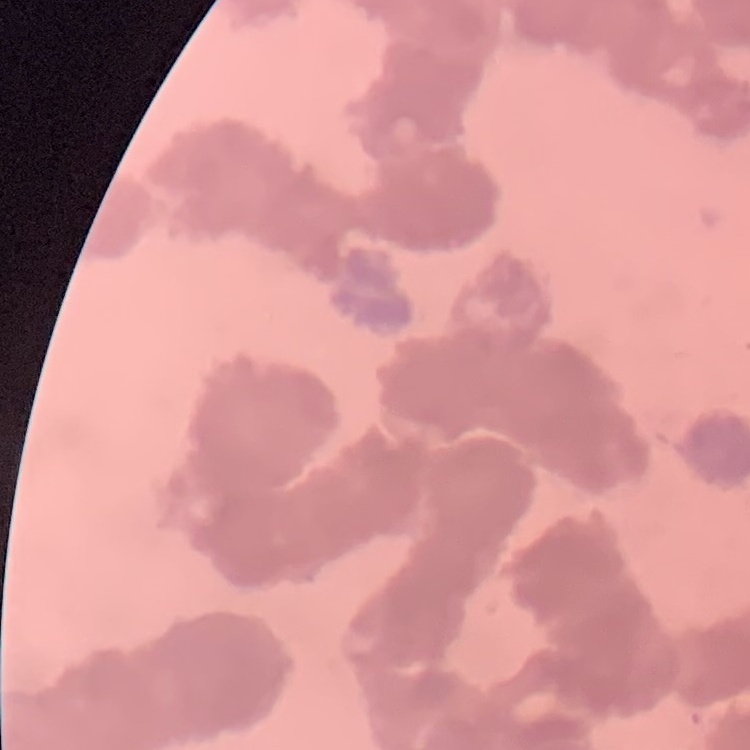

Summary:
  - Red blood cell morphology: rouleaux formation
  - Image type: one tile cut from a larger photomicrograph
  - Stain: Field's or Giemsa
  - Preparation: thin peripheral smear